Classify this cell by malaria status.
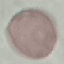

Uninfected.

Automatically extracted cell patch, resized to 64 × 64 pixels. Thin blood film. Photographed with a smartphone camera at the microscope eyepiece. Giemsa-stained preparation.